Locate every Plasmodium parasite.
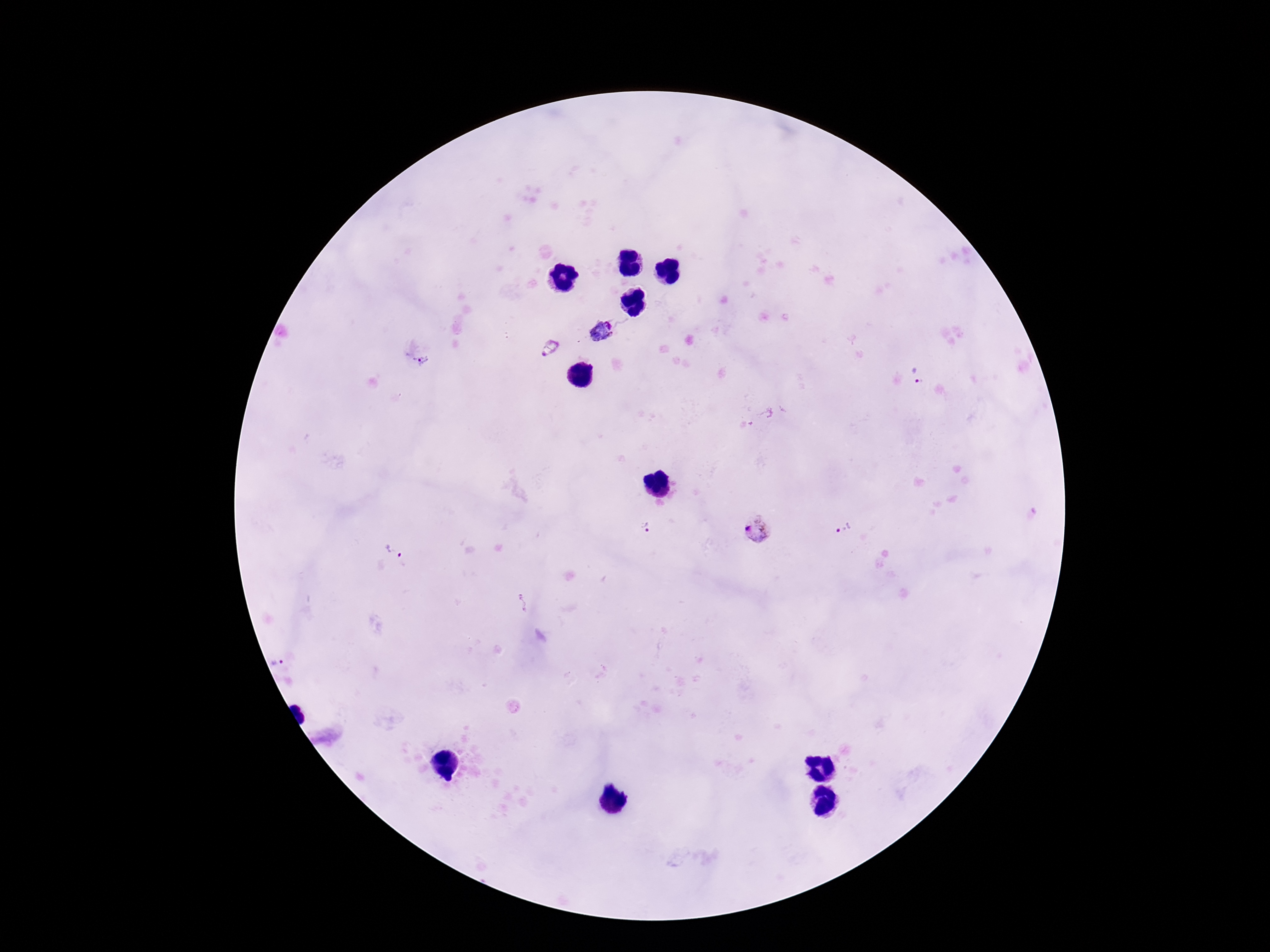
Approximate centers as (x, y) in pixels.
Plasmodium parasites: (603, 334), (550, 348), (423, 360), (915, 375), (646, 525), (758, 527), (845, 529), (393, 552), (522, 604), (283, 664).

Summary:
  - Capture: smartphone camera through the microscope eyepiece
  - Magnification: 100x
  - Patient malaria status: infected
  - Stain: Giemsa
  - Image size: 1270×952 pixels
  - Preparation: thick blood film
  - Field of view: one from this slide